State which parasite is depicted.
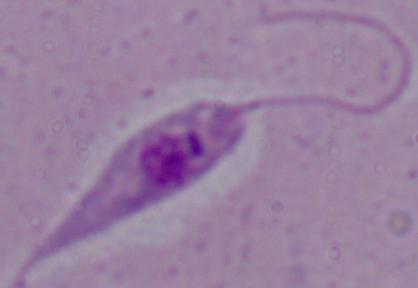
This is Leishmania.

Photomicrograph. 1000x magnification.